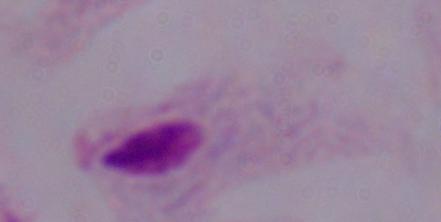

Captured at 1000x magnification. A trichomonad is seen. Photomicrograph.